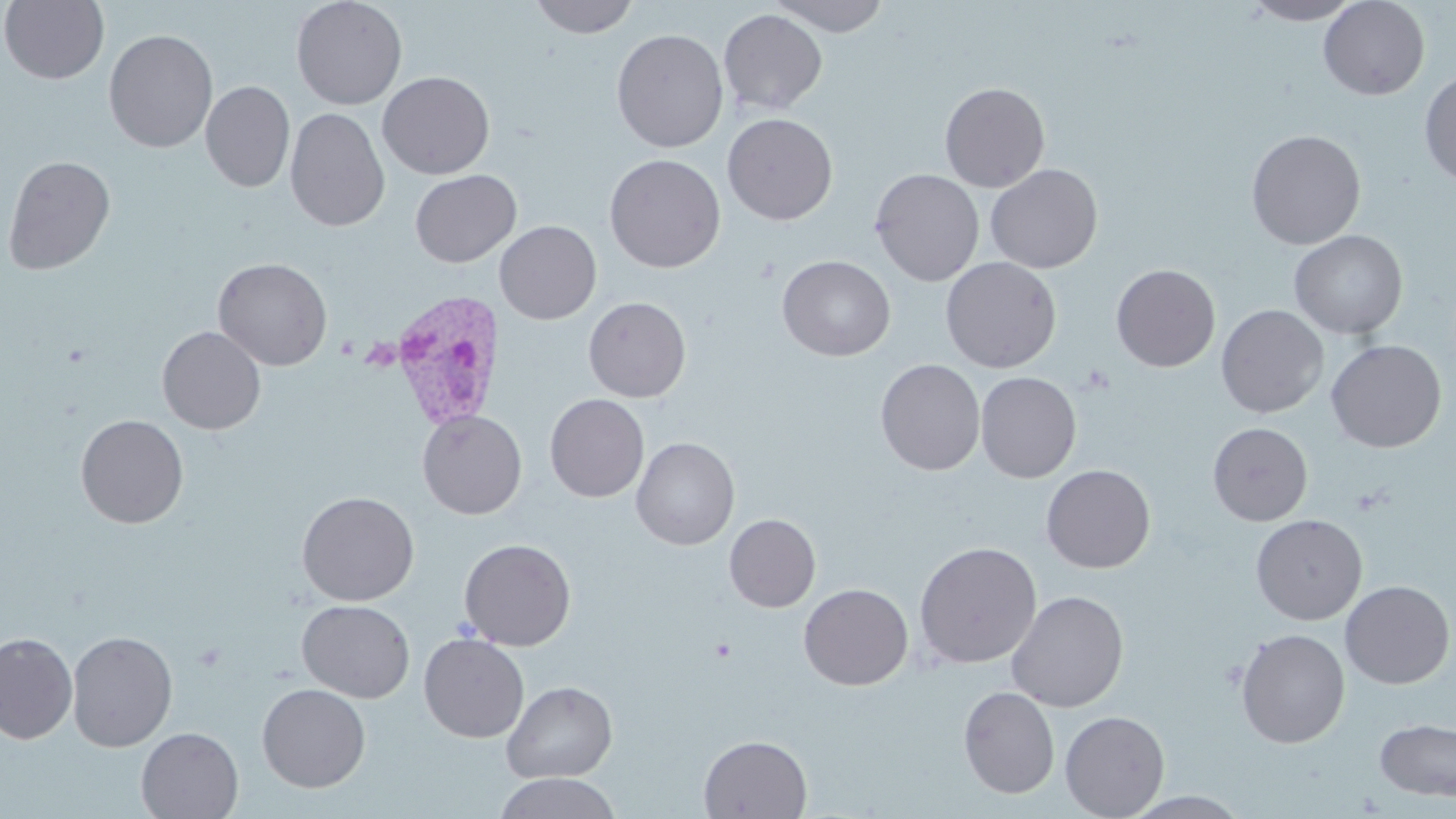

Plasmodium vivax-infected red blood cell locations = approximate bounding boxes as (x1,y1)-(x2,y2) corner pairs in pixels: (387,289)-(505,433)
slide-level diagnosis = Plasmodium vivax
stain = May-Grünwald-Giemsa
field of view = one of a larger specimen
image size = 1456×819 pixels
magnification = 1000x
uninfected red blood cell locations = approximate bounding boxes as (x1,y1)-(x2,y2) corner pairs in pixels: (0,0)-(109,85), (291,0)-(408,110), (528,0)-(639,38), (769,0)-(892,36), (1241,0)-(1363,25), (1319,0)-(1429,100), (718,9)-(827,115), (611,28)-(728,153), (103,29)-(218,153), (1419,69)-(1456,188), (377,71)-(495,179), (201,80)-(295,192), (939,81)-(1050,192), (285,108)-(390,231), (722,113)-(838,225), (1246,129)-(1366,249), (3,154)-(116,275), (605,154)-(726,273), (985,164)-(1104,273), (869,168)-(985,286), (409,169)-(521,267), (495,220)-(601,324), (1289,229)-(1408,339), (777,255)-(895,361), (940,256)-(1062,373), (212,257)-(332,371), (1111,263)-(1220,371), (583,296)-(690,402), (1216,305)-(1329,418), (157,326)-(266,434), (1326,339)-(1447,452), (876,358)-(985,476), (975,371)-(1081,483), (545,394)-(649,502), (417,410)-(527,519), (75,414)-(188,528), (1208,422)-(1313,526), (631,437)-(739,550), (1041,464)-(1156,573), (297,491)-(419,606), (724,513)-(821,612), (1251,514)-(1367,625), (459,538)-(576,650), (914,541)-(1042,669), (1340,580)-(1455,688), (798,583)-(913,690), (1007,590)-(1129,712), (297,600)-(415,703), (1236,628)-(1350,748), (66,630)-(177,752), (0,632)-(77,744), (419,633)-(529,742), (501,680)-(618,783), (257,683)-(371,792), (958,686)-(1059,798), (1060,710)-(1170,818), (1374,718)-(1456,801), (136,727)-(243,819), (699,734)-(812,818), (496,772)-(619,819), (1123,791)-(1251,819)
modality = optical microscopy
preparation = thin blood smear